Classify this cell by malaria status.
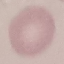

Uninfected.

image_type: automatically extracted cell patch, resized to 64 × 64 pixels
stain: Giemsa
capture: smartphone camera at the microscope eyepiece
preparation: thin smear